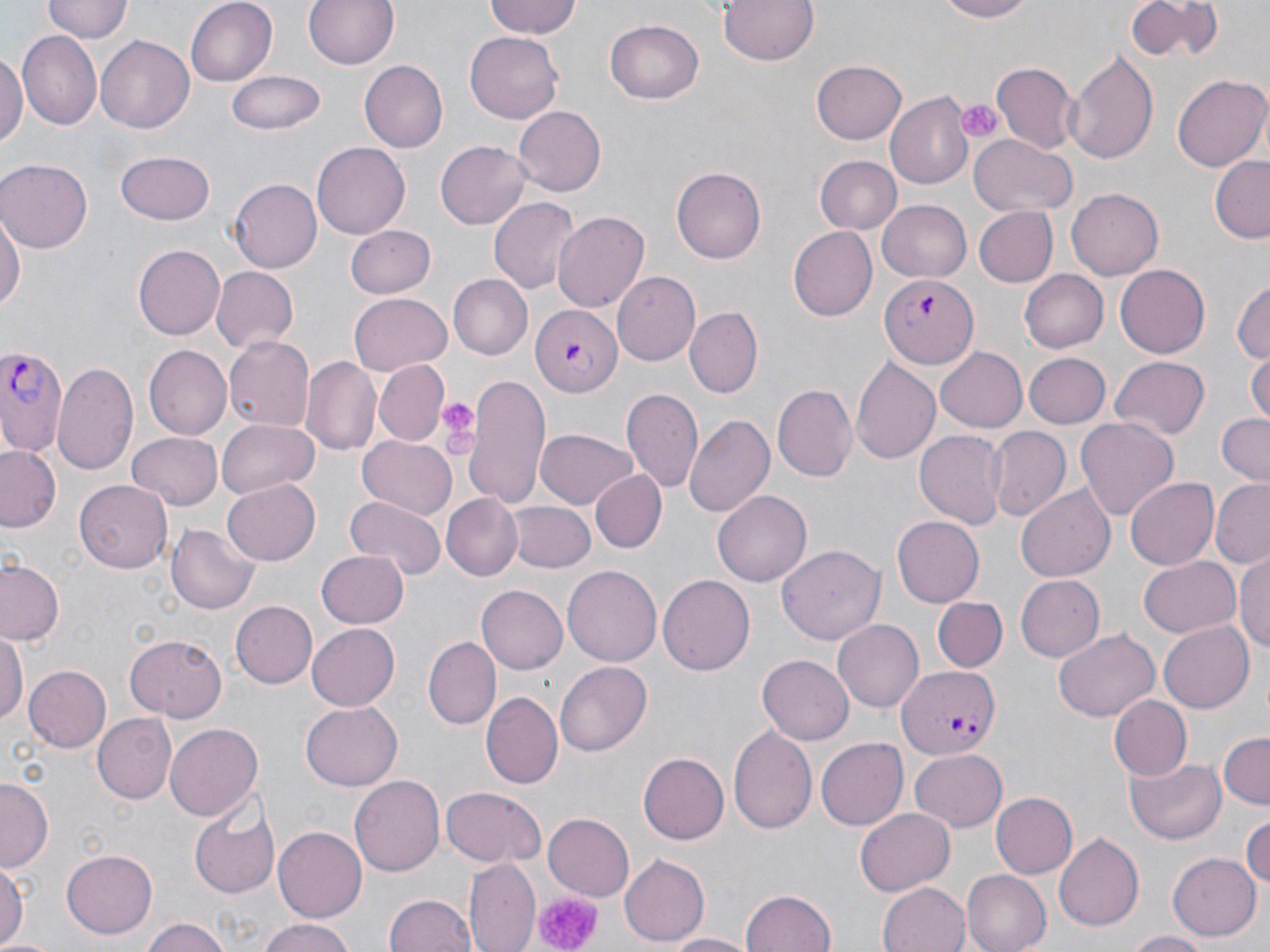
slide_level_diagnosis: Plasmodium falciparum
stain: May-Grünwald-Giemsa
plasmodium_falciparum_infected_red_blood_cell_locations: 'approximate bounding boxes as (x1,y1)-(x2,y2) corner pairs in pixels: (880,271)-(978,368), (533,303)-(623,397), (0,346)-(65,459), (897,663)-(997,759)'
image_size: 1270×952 pixels
uninfected_red_blood_cell_locations: 'approximate bounding boxes as (x1,y1)-(x2,y2) corner pairs in pixels: (42,0)-(130,44), (183,0)-(277,87), (302,0)-(402,73), (484,0)-(582,41), (716,0)-(823,66), (932,0)-(1035,23), (1121,0)-(1225,63), (605,19)-(705,104), (466,29)-(564,121), (19,30)-(102,127), (96,34)-(195,133), (1065,47)-(1161,165), (0,54)-(26,150), (811,59)-(908,146), (359,60)-(448,154), (993,64)-(1077,151), (228,71)-(325,135), (1172,75)-(1269,171), (884,94)-(973,188), (514,105)-(606,196), (968,134)-(1076,216), (436,141)-(531,230), (313,143)-(410,237), (114,150)-(216,227), (1210,154)-(1270,244), (817,155)-(902,235), (0,160)-(91,250), (672,167)-(767,263), (230,179)-(322,272), (1067,188)-(1164,281), (488,195)-(578,295), (878,199)-(973,281), (974,207)-(1058,287), (0,209)-(24,321), (551,212)-(651,312), (345,225)-(435,299), (787,227)-(876,321), (136,229)-(230,420), (134,246)-(224,338), (1115,263)-(1210,358), (210,266)-(296,353), (1021,269)-(1109,353), (611,271)-(702,364), (449,276)-(532,359), (1231,277)-(1270,367), (348,293)-(452,375), (685,308)-(762,396), (223,336)-(315,430), (144,346)-(231,440), (934,348)-(1029,432), (1249,352)-(1270,429), (1023,353)-(1112,428), (301,357)-(381,459), (850,357)-(942,467), (1110,357)-(1212,441), (373,361)-(449,445), (54,362)-(142,476), (463,376)-(551,510), (772,383)-(858,482), (621,390)-(703,495), (1215,412)-(1270,485), (684,415)-(774,520), (1076,417)-(1180,522), (218,419)-(319,496), (915,427)-(1008,528), (988,427)-(1069,522), (536,429)-(638,510), (127,431)-(224,508), (357,436)-(457,521), (0,445)-(60,531), (591,471)-(666,552), (1125,478)-(1218,569), (1209,480)-(1270,567), (75,481)-(172,573), (223,481)-(319,564), (1017,485)-(1116,582), (712,492)-(812,585), (441,494)-(523,580), (346,497)-(446,582), (507,501)-(595,573), (894,515)-(985,608), (166,524)-(259,615), (776,543)-(886,645), (316,550)-(408,628), (1235,552)-(1270,659), (0,556)-(65,648), (1137,556)-(1240,640), (562,565)-(661,668), (658,575)-(753,677), (1014,575)-(1104,663), (476,585)-(568,674), (932,596)-(1007,673), (231,601)-(318,689), (834,618)-(924,711), (1158,620)-(1257,712), (307,623)-(400,710), (1054,628)-(1159,722), (0,630)-(25,728), (124,634)-(226,722), (424,637)-(500,729), (759,656)-(852,744), (553,660)-(652,758), (24,666)-(112,752), (481,692)-(563,789), (1107,695)-(1192,782), (301,702)-(404,790), (91,713)-(176,803), (165,723)-(262,821), (727,724)-(817,833), (1217,732)-(1270,809), (816,738)-(907,830), (910,747)-(1009,831), (640,750)-(730,844), (1125,756)-(1228,844), (349,776)-(445,876), (0,779)-(51,873), (441,787)-(546,868), (992,793)-(1078,878), (190,799)-(280,898), (854,806)-(955,895), (543,812)-(635,900), (1243,813)-(1270,890), (274,826)-(366,919), (1055,829)-(1144,931), (61,851)-(157,938), (1167,853)-(1260,941), (618,856)-(709,946), (464,857)-(539,952), (0,862)-(28,946), (961,869)-(1053,952), (878,880)-(970,952), (738,890)-(836,952), (385,894)-(476,952), (140,916)-(233,952), (258,921)-(359,952), (1121,930)-(1217,952), (662,931)-(757,952)'
platelet_locations: 'approximate bounding boxes as (x1,y1)-(x2,y2) corner pairs in pixels: (955,97)-(1001,145), (434,396)-(483,452), (530,889)-(600,952)'
magnification: 1000x
field_of_view: single
preparation: thin blood smear
modality: optical microscopy